Name the parasite shown.
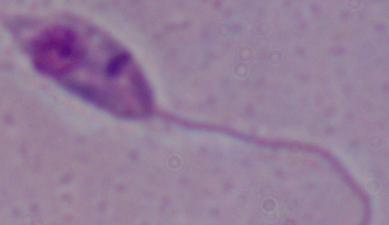
This is Leishmania.

Photomicrograph. 1000x magnification.